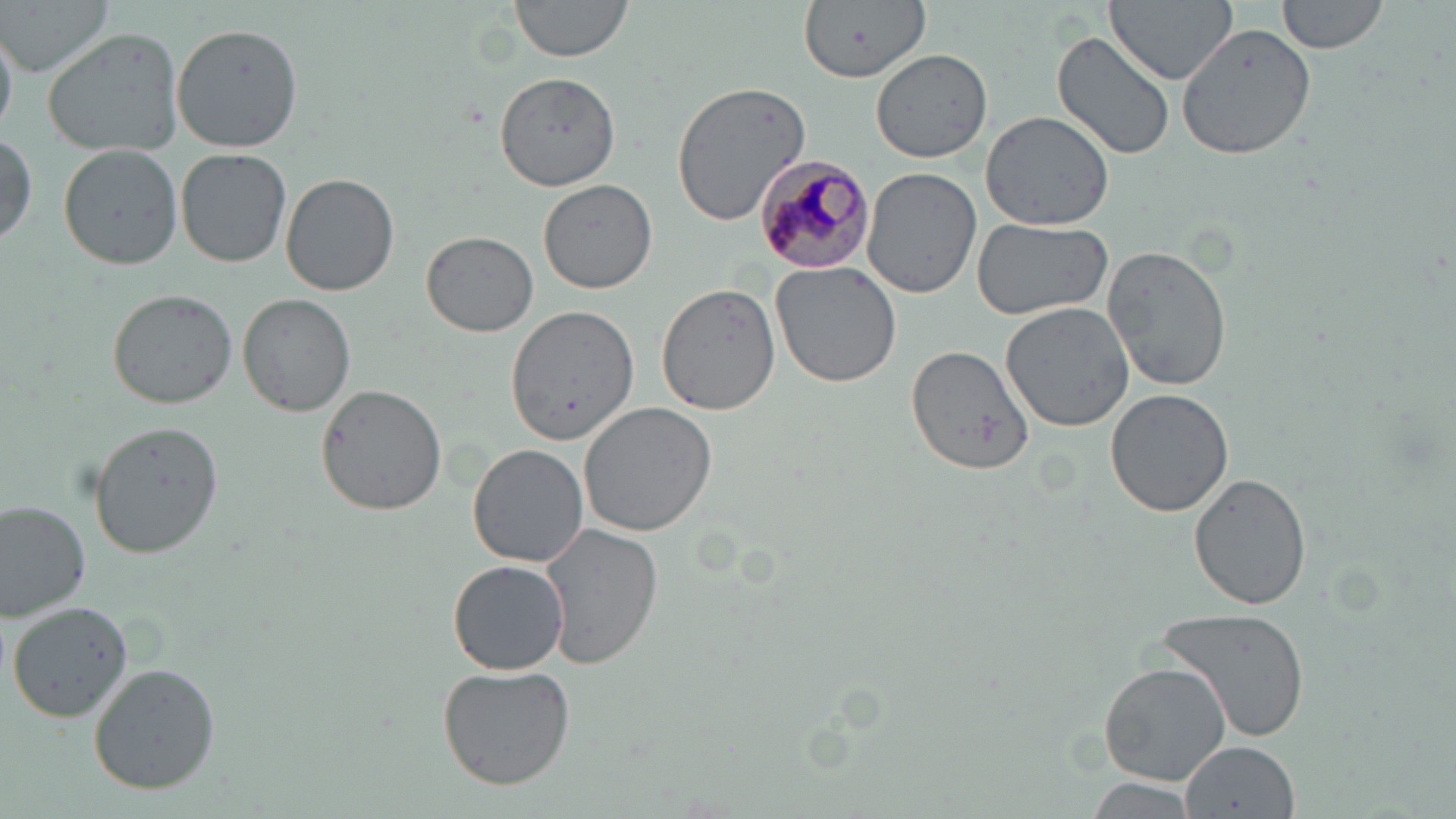 Approximate bounding boxes as named x1/y1/x2/y2 corners in pixels. Plasmodium malariae-infected red blood cell locations: (x1=757, y1=152, x2=876, y2=274). Uninfected red blood cell locations: (x1=3, y1=0, x2=114, y2=76), (x1=508, y1=0, x2=635, y2=65), (x1=796, y1=0, x2=932, y2=84), (x1=1107, y1=0, x2=1237, y2=84), (x1=1275, y1=0, x2=1388, y2=55), (x1=1175, y1=19, x2=1318, y2=159), (x1=172, y1=23, x2=301, y2=151), (x1=0, y1=26, x2=17, y2=134), (x1=42, y1=29, x2=186, y2=156), (x1=1052, y1=30, x2=1175, y2=161), (x1=871, y1=48, x2=993, y2=164), (x1=490, y1=76, x2=620, y2=188), (x1=668, y1=79, x2=813, y2=224), (x1=980, y1=107, x2=1118, y2=231), (x1=0, y1=132, x2=38, y2=249), (x1=59, y1=144, x2=184, y2=268), (x1=175, y1=147, x2=292, y2=266), (x1=863, y1=169, x2=982, y2=298), (x1=281, y1=174, x2=399, y2=296), (x1=537, y1=177, x2=657, y2=294), (x1=972, y1=217, x2=1112, y2=321), (x1=420, y1=230, x2=538, y2=338), (x1=1101, y1=243, x2=1232, y2=394), (x1=770, y1=261, x2=904, y2=388), (x1=656, y1=283, x2=781, y2=415), (x1=107, y1=287, x2=237, y2=409), (x1=238, y1=292, x2=356, y2=417), (x1=1000, y1=302, x2=1136, y2=431), (x1=505, y1=307, x2=639, y2=442), (x1=907, y1=344, x2=1034, y2=475), (x1=316, y1=384, x2=448, y2=515), (x1=1105, y1=390, x2=1234, y2=517), (x1=579, y1=403, x2=719, y2=537), (x1=89, y1=419, x2=226, y2=556), (x1=468, y1=442, x2=591, y2=569), (x1=1187, y1=472, x2=1313, y2=613), (x1=0, y1=501, x2=91, y2=622), (x1=542, y1=522, x2=663, y2=670), (x1=446, y1=560, x2=569, y2=676), (x1=5, y1=600, x2=133, y2=724), (x1=1154, y1=606, x2=1311, y2=745), (x1=87, y1=662, x2=220, y2=794), (x1=1099, y1=662, x2=1229, y2=785), (x1=436, y1=664, x2=576, y2=789), (x1=1181, y1=740, x2=1298, y2=816), (x1=1084, y1=779, x2=1198, y2=817). Slide-level diagnosis: Plasmodium malariae. May-Grünwald-Giemsa-stained preparation. Single field of view. Captured at 1000x magnification. Optical microscopy. Image is 1456×819 pixels. Thin blood film.